Point out each leukocyte.
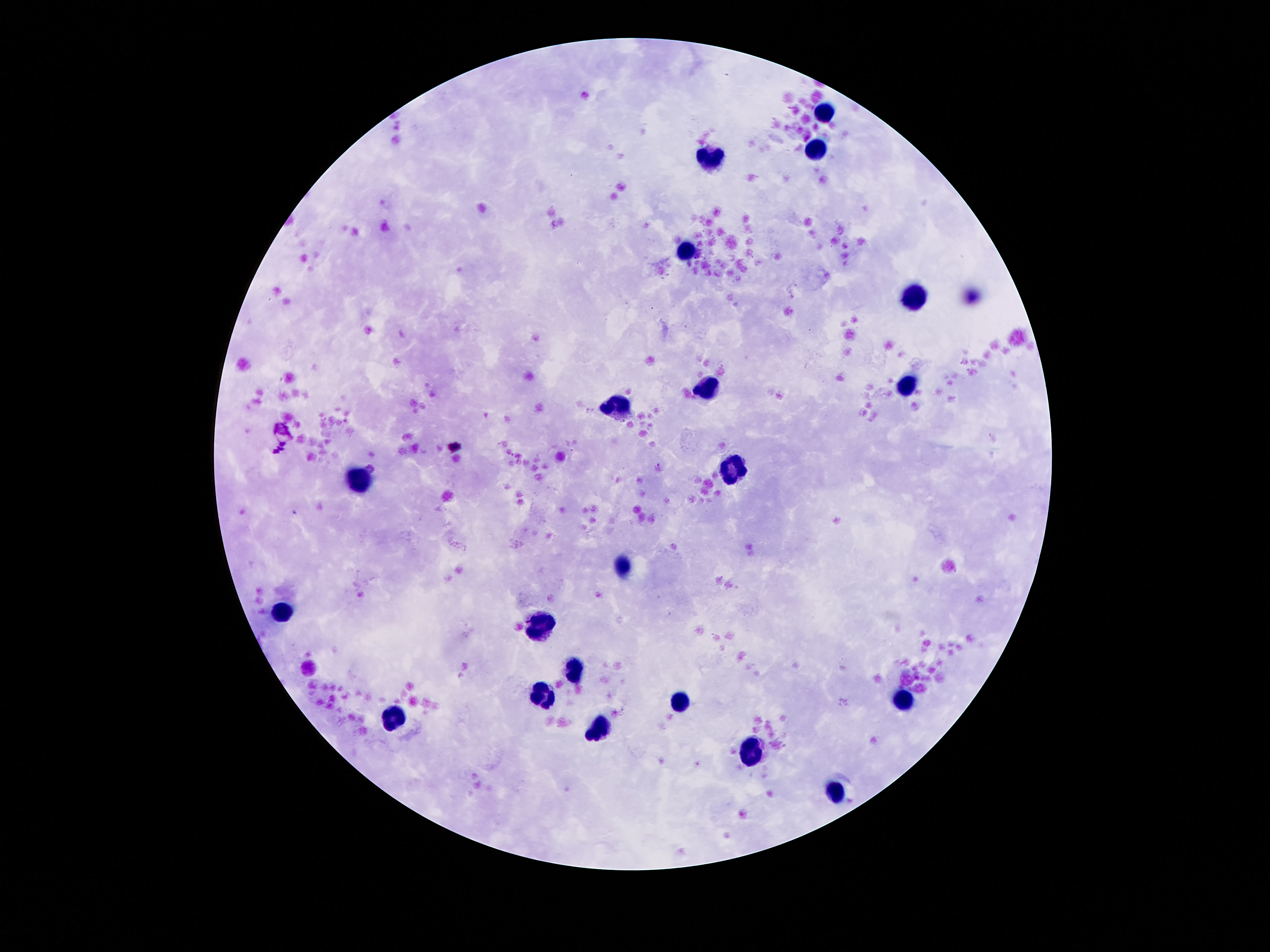
Approximate centers as {x, y} in pixels.
Leukocytes: {827, 112}, {817, 147}, {709, 162}, {687, 250}, {914, 297}, {707, 388}, {909, 388}, {621, 403}, {735, 468}, {360, 482}, {625, 564}, {283, 610}, {541, 627}, {575, 672}, {545, 697}, {675, 702}, {901, 702}, {395, 717}, {601, 731}, {752, 756}, {838, 789}.

Giemsa stain. Patient malaria status: uninfected. One field from this slide. 100x magnification. Smartphone photograph taken through the microscope eyepiece. Image is 1270×952 pixels. Thick blood film.